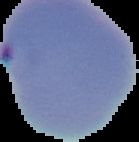

Summary:
  - Image size: 139×142 pixels
  - Preparation: thin blood film
  - Image type: segmented cell region on a black background
  - Result: malaria parasites identified